Locate and identify every blood parasite.
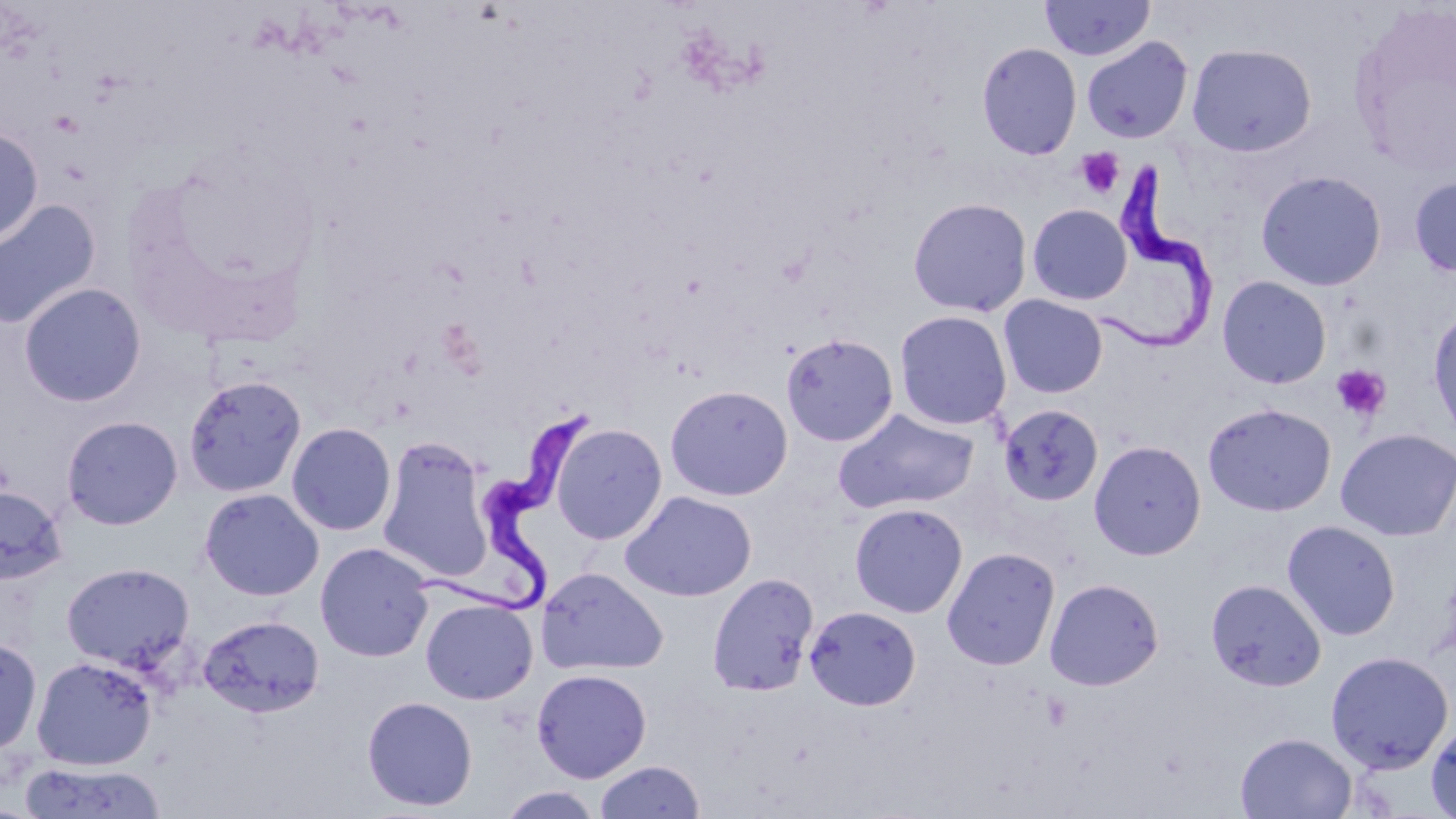
Approximate bounding boxes as named x1/y1/x2/y2 corners in pixels.
Trypanosoma brucei: (x1=1094, y1=157, x2=1213, y2=357), (x1=417, y1=404, x2=603, y2=620).
No Plasmodium falciparum, Plasmodium ovale, Plasmodium malariae, Plasmodium vivax, or Babesia divergens observed.

Uninfected red blood cell locations: (x1=1039, y1=0, x2=1155, y2=62), (x1=1081, y1=36, x2=1193, y2=144), (x1=976, y1=42, x2=1082, y2=160), (x1=1186, y1=43, x2=1317, y2=157), (x1=0, y1=126, x2=43, y2=247), (x1=1255, y1=169, x2=1388, y2=291), (x1=1408, y1=176, x2=1456, y2=278), (x1=907, y1=197, x2=1033, y2=317), (x1=0, y1=198, x2=102, y2=331), (x1=1027, y1=203, x2=1133, y2=306), (x1=1217, y1=275, x2=1333, y2=389), (x1=18, y1=282, x2=146, y2=408), (x1=998, y1=294, x2=1109, y2=399), (x1=1428, y1=307, x2=1456, y2=446), (x1=893, y1=309, x2=1013, y2=431), (x1=781, y1=332, x2=898, y2=447), (x1=183, y1=374, x2=307, y2=499), (x1=664, y1=384, x2=793, y2=501), (x1=1202, y1=402, x2=1337, y2=517), (x1=998, y1=403, x2=1104, y2=508), (x1=832, y1=408, x2=980, y2=515), (x1=61, y1=415, x2=183, y2=529), (x1=286, y1=422, x2=397, y2=536), (x1=550, y1=423, x2=667, y2=544), (x1=1336, y1=427, x2=1456, y2=541), (x1=377, y1=436, x2=493, y2=584), (x1=1088, y1=440, x2=1206, y2=560), (x1=0, y1=485, x2=68, y2=586), (x1=198, y1=488, x2=324, y2=601), (x1=621, y1=490, x2=757, y2=602), (x1=849, y1=502, x2=968, y2=618), (x1=1282, y1=520, x2=1402, y2=641), (x1=315, y1=542, x2=435, y2=662), (x1=941, y1=547, x2=1061, y2=670), (x1=60, y1=562, x2=195, y2=673), (x1=537, y1=568, x2=668, y2=675), (x1=706, y1=572, x2=819, y2=698), (x1=1044, y1=578, x2=1164, y2=690), (x1=1205, y1=578, x2=1326, y2=691), (x1=420, y1=598, x2=538, y2=705), (x1=804, y1=605, x2=921, y2=711), (x1=198, y1=614, x2=325, y2=719), (x1=0, y1=634, x2=42, y2=757), (x1=1325, y1=650, x2=1455, y2=773), (x1=31, y1=656, x2=157, y2=770), (x1=532, y1=668, x2=652, y2=782), (x1=361, y1=695, x2=478, y2=811), (x1=1425, y1=717, x2=1456, y2=819), (x1=1235, y1=731, x2=1358, y2=818), (x1=594, y1=759, x2=705, y2=819), (x1=18, y1=760, x2=167, y2=819), (x1=497, y1=786, x2=605, y2=819). Platelet locations: (x1=1076, y1=147, x2=1125, y2=199), (x1=1331, y1=363, x2=1391, y2=422). Slide-level diagnosis: Trypanosoma brucei. Light microscopy. Image is 1456×819 pixels. One field of a larger specimen. Thin blood film. Captured at 1000x magnification. May-Grünwald-Giemsa stain.